Identify the parasite.
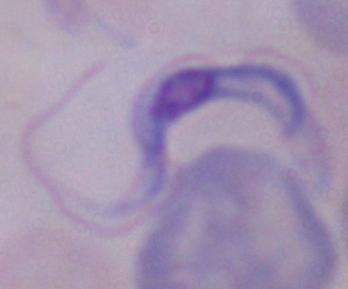
A trypanosome.

modality = photomicrograph
magnification = 1000x